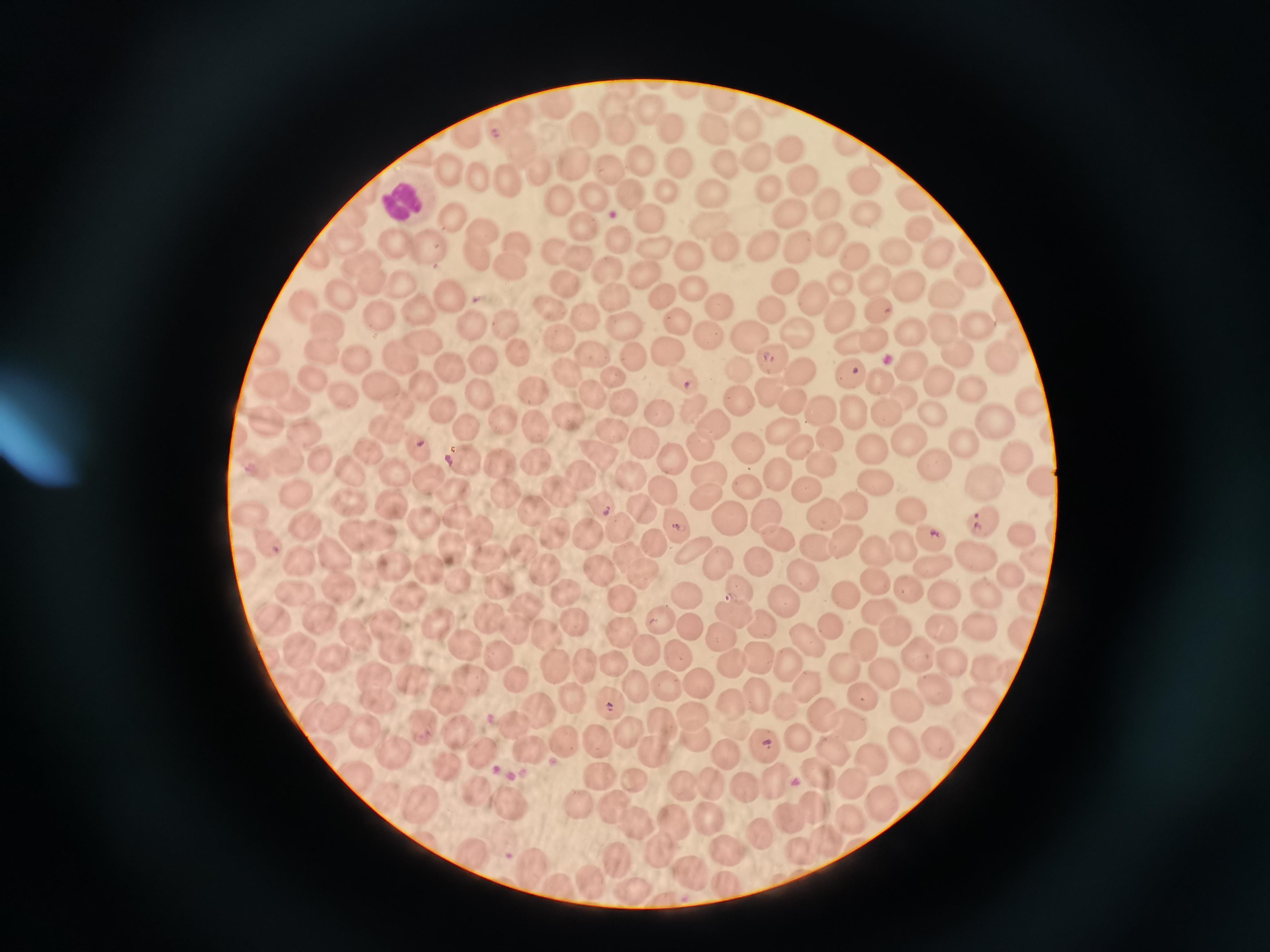

Approximate centers as {x, y} in pixels.
Summary:
  - Cell locations: {553, 107}, {614, 107}, {652, 109}, {521, 120}, {747, 124}, {583, 127}, {667, 127}, {618, 129}, {713, 129}, {503, 132}, {467, 135}, {520, 144}, {787, 148}, {756, 153}, {637, 161}, {675, 162}, {574, 163}, {724, 163}, {539, 166}, {606, 167}, {448, 169}, {483, 177}, {504, 179}, {805, 182}, {864, 182}, {767, 184}, {667, 188}, {632, 194}, {712, 194}, {591, 195}, {913, 195}, {827, 201}, {558, 202}, {862, 210}, {353, 213}, {790, 215}, {650, 216}, {453, 218}, {581, 225}, {918, 225}, {710, 230}, {486, 232}, {615, 237}, {829, 237}, {344, 241}, {515, 241}, {392, 242}, {760, 245}, {797, 246}, {427, 248}, {896, 249}, {722, 250}, {652, 251}, {554, 252}, {473, 253}, {935, 253}, {578, 257}, {686, 258}, {851, 258}, {506, 262}, {363, 265}, {606, 267}, {967, 269}, {644, 271}, {786, 275}, {375, 279}, {883, 283}, {838, 285}, {404, 287}, {690, 288}, {913, 288}, {563, 289}, {449, 291}, {942, 291}, {342, 295}, {812, 295}, {659, 297}, {614, 298}, {307, 306}, {721, 306}, {771, 306}, {881, 306}, {1003, 307}, {549, 308}, {380, 312}, {421, 312}, {839, 314}, {585, 318}, {502, 322}, {468, 323}, {675, 323}, {327, 325}, {620, 325}, {940, 325}, {977, 327}, {708, 332}, {795, 332}, {875, 334}, {746, 336}, {908, 336}, {1018, 338}, {425, 339}, {560, 339}, {853, 342}, {665, 346}, {952, 349}, {398, 350}, {590, 350}, {268, 351}, {323, 351}, {483, 351}, {515, 352}, {630, 357}, {1000, 357}, {358, 358}, {770, 360}, {909, 367}, {739, 368}, {850, 368}, {453, 369}, {803, 370}, {314, 373}, {568, 375}, {684, 375}, {613, 379}, {880, 380}, {972, 384}, {938, 385}, {374, 386}, {424, 387}, {769, 388}, {277, 389}, {535, 390}, {591, 394}, {479, 395}, {1029, 395}, {339, 397}, {793, 397}, {298, 399}, {904, 399}, {688, 400}, {738, 400}, {625, 405}, {852, 405}, {393, 406}, {818, 407}, {656, 408}, {442, 410}, {935, 412}, {503, 415}, {885, 415}, {567, 418}, {533, 419}, {993, 420}, {264, 422}, {298, 426}, {714, 427}, {777, 427}, {607, 430}, {466, 431}, {384, 432}, {827, 435}, {642, 440}, {907, 441}, {960, 444}, {698, 445}, {746, 445}, {800, 446}, {415, 448}, {371, 449}, {670, 451}, {867, 451}, {598, 453}, {284, 457}, {535, 458}, {820, 458}, {1019, 458}, {321, 459}, {463, 459}, {498, 463}, {928, 463}, {628, 471}, {774, 471}, {356, 473}, {392, 473}, {425, 474}, {706, 474}, {577, 476}, {1042, 477}, {985, 480}, {871, 482}, {745, 483}, {658, 488}, {502, 489}, {559, 489}, {802, 490}, {297, 492}, {454, 493}, {704, 493}, {600, 501}, {851, 502}, {391, 503}, {347, 505}, {635, 505}, {912, 507}, {532, 509}, {822, 510}, {458, 512}, {760, 513}, {250, 514}, {722, 514}, {419, 520}, {984, 521}, {613, 524}, {305, 525}, {674, 527}, {588, 530}, {378, 531}, {481, 531}, {353, 532}, {926, 532}, {773, 534}, {552, 535}, {1017, 536}, {840, 541}, {264, 543}, {450, 543}, {905, 543}, {656, 544}, {813, 545}, {524, 546}, {692, 549}, {335, 553}, {879, 555}, {628, 556}, {977, 556}, {1035, 557}, {488, 558}, {300, 561}, {392, 561}, {759, 562}, {930, 562}, {426, 565}, {714, 566}, {549, 568}, {1010, 572}, {600, 575}, {803, 576}, {639, 577}, {873, 578}, {458, 581}, {499, 583}, {336, 584}, {906, 585}, {294, 588}, {736, 589}, {566, 592}, {616, 595}, {943, 595}, {847, 596}, {987, 596}, {406, 600}, {684, 600}, {1029, 600}, {779, 604}, {527, 605}, {880, 609}, {735, 610}, {273, 614}, {487, 615}, {320, 618}, {657, 620}, {386, 622}, {438, 624}, {688, 624}, {977, 624}, {576, 626}, {511, 627}, {761, 628}, {831, 629}, {941, 629}, {544, 631}, {893, 631}, {617, 633}, {718, 633}, {1022, 634}, {354, 635}, {807, 638}, {466, 644}, {650, 644}, {862, 645}, {300, 649}, {396, 649}, {923, 652}, {503, 656}, {757, 657}, {336, 658}, {677, 658}, {947, 661}, {732, 662}, {616, 663}, {584, 664}, {791, 665}, {557, 666}, {983, 671}, {838, 673}, {887, 675}, {472, 677}, {371, 678}, {412, 678}, {805, 682}, {516, 683}, {696, 683}, {669, 684}, {313, 685}, {633, 687}, {935, 689}, {864, 694}, {977, 695}, {374, 696}, {755, 696}, {453, 698}, {607, 700}, {573, 701}, {730, 702}, {903, 703}, {783, 704}, {820, 712}, {537, 713}, {330, 714}, {688, 714}, {849, 721}, {516, 727}, {663, 728}, {628, 729}, {365, 731}, {424, 731}, {463, 736}, {799, 738}, {596, 740}, {696, 740}, {560, 742}, {901, 743}, {766, 744}, {931, 744}, {528, 749}, {649, 749}, {831, 749}, {395, 751}, {480, 751}, {727, 754}, {867, 755}, {358, 769}, {815, 769}, {596, 772}, {772, 777}, {633, 780}, {682, 781}, {706, 782}, {851, 783}, {915, 786}, {742, 788}, {480, 793}, {508, 799}, {576, 801}, {879, 802}, {421, 803}, {814, 805}, {607, 809}, {849, 816}, {708, 818}, {787, 819}, {636, 825}, {669, 825}, {759, 831}, {824, 837}, {474, 850}, {728, 851}, {659, 853}, {799, 854}, {618, 858}, {531, 863}, {689, 871}, {727, 879}, {591, 881}, {631, 888}, {562, 890}
  - Malaria reading: positive
  - Stain: Giemsa
  - Preparation: thin blood film
  - Capture: smartphone through the microscope eyepiece
  - Image size: 1270×952 pixels
  - Field of view: single